Locate every Plasmodium parasite.
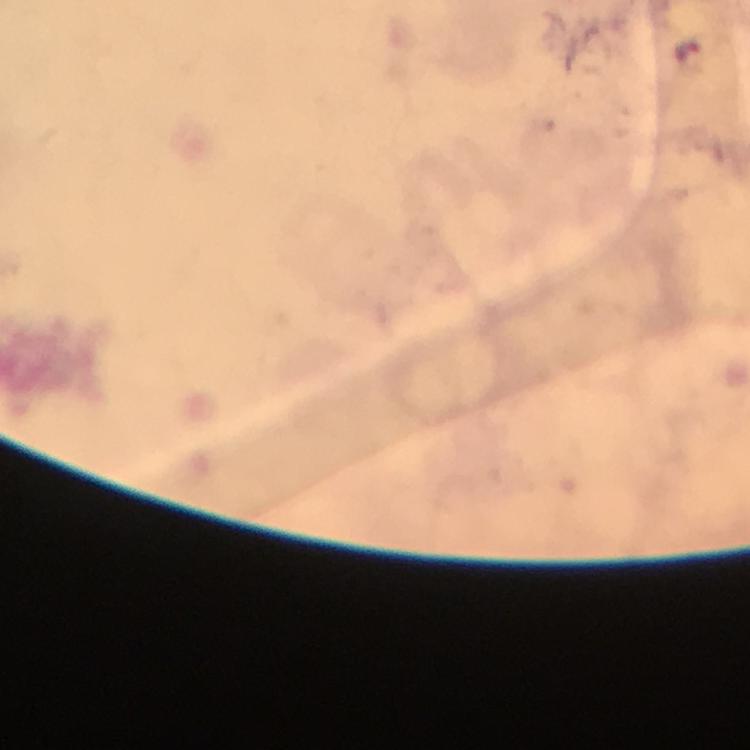

Approximate centers as {x, y} in pixels.
Plasmodium parasites: {685, 48}.

Cropped region of a single field of view. At 100x magnification. Giemsa stain. Image is 750×750 pixels. Immersion oil was used. Smartphone photograph taken through a microscope. From a malaria diagnostic workup. Thick blood smear.